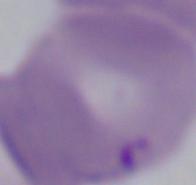

A Babesia parasite is shown. 1000x magnification. Photomicrograph.